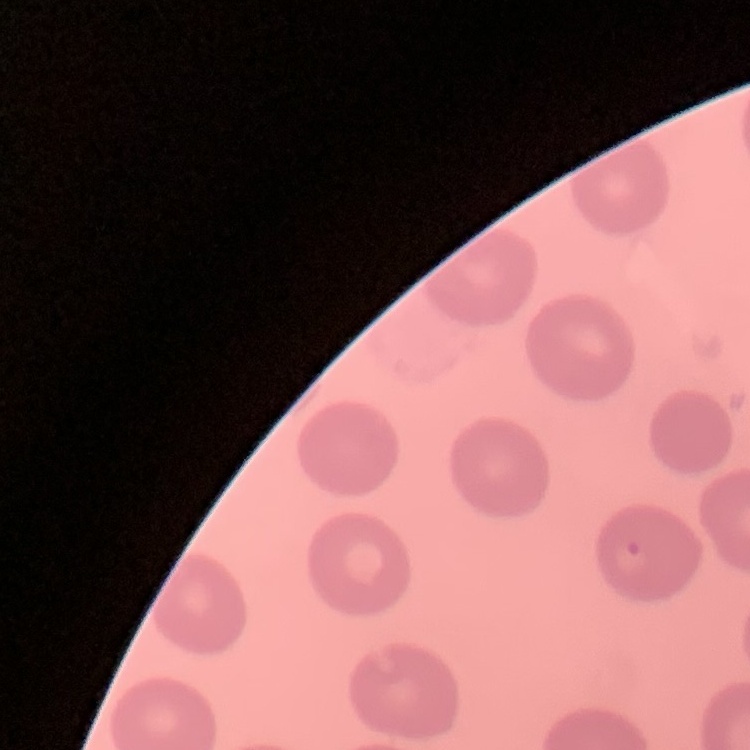

The red blood cells show no rouleaux formation. Thin peripheral smear. One tile cut from a larger photomicrograph. Field's or Giemsa stain.